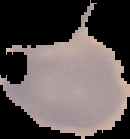

{
  "result": "no malaria parasites detected",
  "image_size": "130×139 pixels",
  "preparation": "thin blood smear",
  "image_type": "cell region segmented out of the field of view; surrounding area masked to black"
}